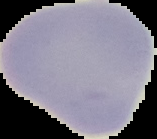

Summary:
  - Image type: segmented cell region with the area outside set to black
  - Preparation: thin blood smear
  - Result: no Plasmodium parasites detected
  - Image size: 157×139 pixels